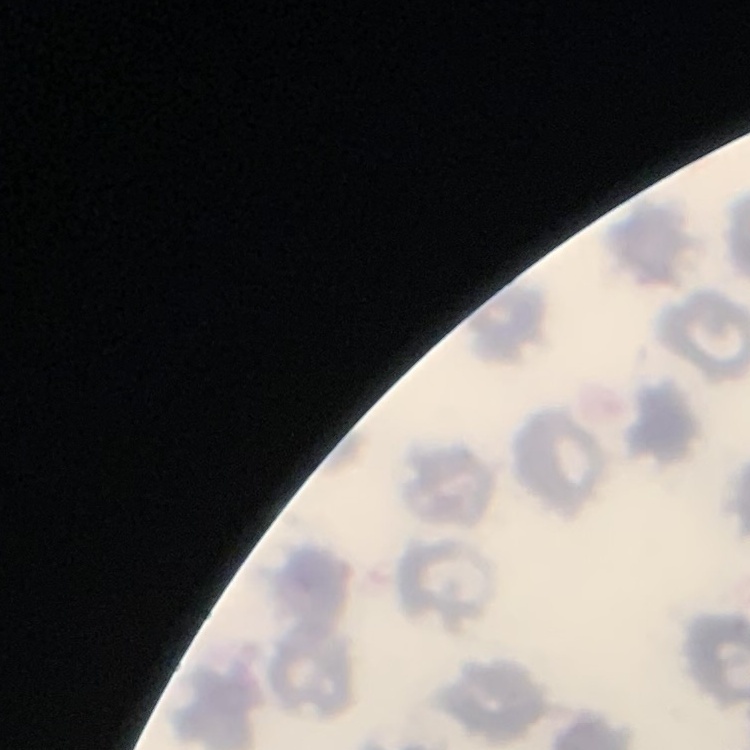

Summary:
  - Red blood cell morphology: no rouleaux formation
  - Stain: Field's or Giemsa
  - Image type: square crop of a larger photomicrograph
  - Preparation: thin blood smear